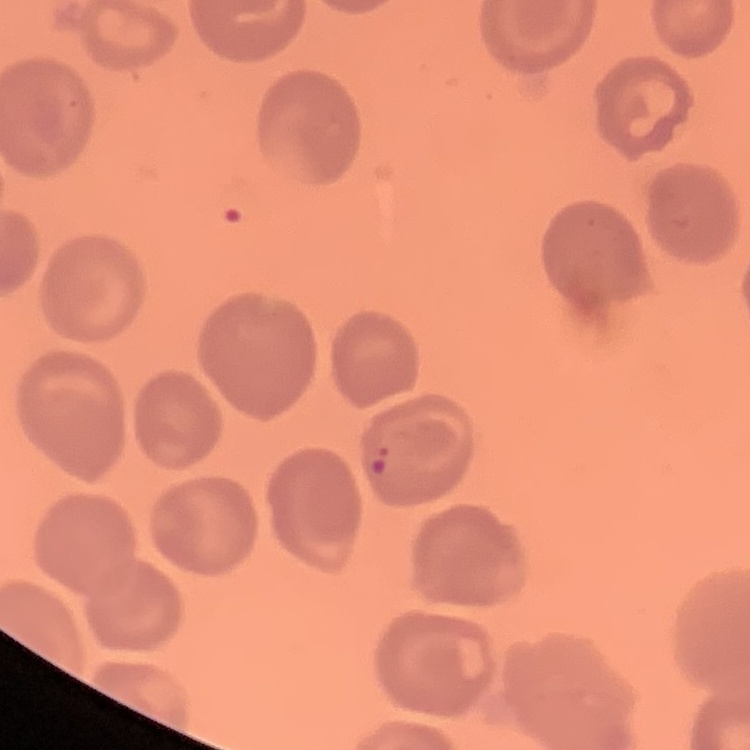

erythrocyte morphology = no rouleaux formation
stain = Field's or Giemsa
image type = one tile cut from a larger photomicrograph
preparation = thin peripheral smear